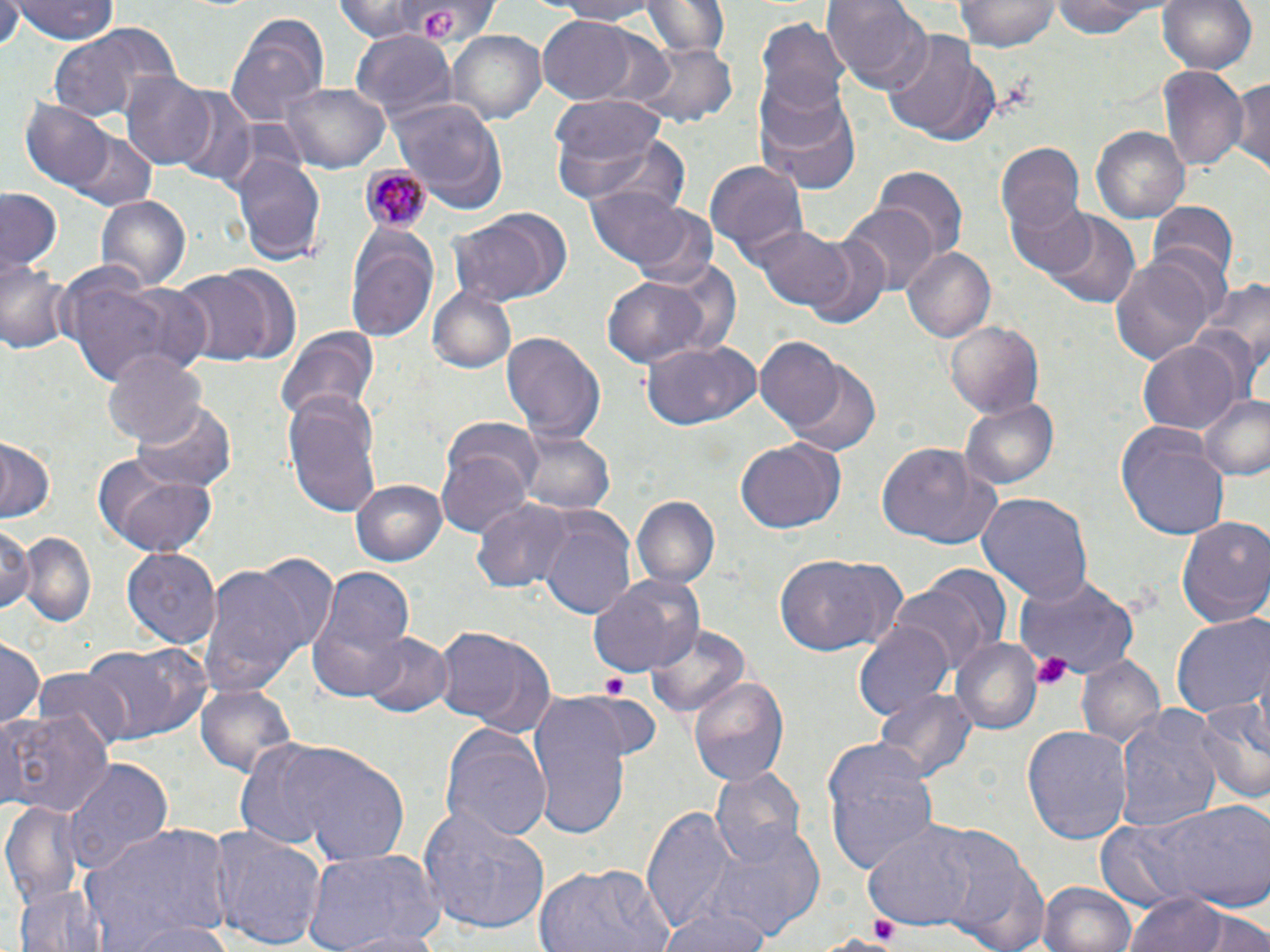

slide-level diagnosis = Plasmodium malariae
magnification = 1000x
platelet locations = approximate bounding boxes as (x1, y1, x2, y2) in pixels: (422, 7, 461, 41), (1034, 651, 1074, 690), (601, 673, 631, 696), (869, 914, 902, 946)
Plasmodium malariae-infected red blood cell locations = approximate bounding boxes as (x1, y1, x2, y2) in pixels: (361, 168, 429, 235)
stain = May-Grünwald-Giemsa
modality = light microscopy
field of view = single
uninfected red blood cell locations = approximate bounding boxes as (x1, y1, x2, y2) in pixels: (328, 0, 471, 43), (548, 0, 671, 25), (644, 0, 728, 58), (823, 0, 931, 93), (957, 0, 1061, 52), (1048, 0, 1172, 39), (1159, 0, 1257, 77), (9, 1, 121, 45), (0, 4, 24, 50), (225, 11, 331, 126), (537, 16, 642, 103), (755, 20, 850, 119), (448, 28, 549, 124), (44, 30, 149, 121), (352, 31, 454, 121), (879, 36, 997, 146), (633, 43, 736, 127), (1157, 65, 1246, 173), (1232, 71, 1270, 178), (119, 74, 216, 169), (282, 82, 390, 171), (755, 85, 862, 195), (171, 90, 256, 187), (551, 93, 669, 202), (387, 94, 507, 214), (21, 102, 113, 190), (1091, 126, 1189, 221), (580, 132, 694, 219), (64, 133, 156, 210), (994, 139, 1086, 238), (230, 149, 326, 267), (705, 159, 808, 259), (874, 164, 968, 262), (583, 183, 704, 277), (1, 190, 63, 271), (95, 195, 190, 293), (1004, 195, 1097, 280), (842, 202, 941, 293), (1151, 203, 1237, 286), (620, 205, 720, 294), (448, 209, 572, 306), (1043, 212, 1141, 307), (345, 224, 437, 339), (746, 224, 855, 313), (798, 231, 894, 331), (901, 246, 995, 344), (1108, 254, 1217, 368), (0, 256, 73, 358), (646, 258, 746, 356), (169, 263, 300, 373), (51, 265, 200, 388), (601, 274, 711, 370), (1192, 281, 1270, 402), (426, 283, 518, 374), (943, 319, 1044, 419), (274, 328, 378, 428), (502, 330, 606, 441), (753, 336, 851, 436), (642, 337, 763, 431), (1137, 338, 1243, 436), (102, 349, 206, 447), (780, 360, 882, 460), (283, 391, 383, 518), (1196, 393, 1270, 480), (960, 395, 1059, 489), (133, 401, 236, 494), (446, 419, 547, 498), (1116, 424, 1232, 541), (514, 427, 613, 518), (0, 437, 57, 522), (735, 439, 845, 533), (439, 442, 533, 537), (873, 443, 1002, 549), (94, 459, 217, 559), (353, 480, 447, 565), (976, 493, 1092, 610), (631, 494, 719, 589), (474, 500, 577, 593), (538, 509, 637, 623), (1176, 514, 1270, 628), (1, 523, 38, 616), (15, 531, 96, 630), (124, 548, 220, 650), (239, 548, 340, 657), (773, 554, 905, 659), (197, 560, 312, 696), (307, 569, 411, 699), (585, 572, 695, 679), (1013, 572, 1141, 678), (888, 581, 996, 678), (1173, 614, 1270, 719), (647, 622, 752, 722), (853, 622, 954, 725), (435, 627, 558, 737), (360, 632, 453, 718), (80, 636, 211, 744), (0, 639, 45, 725), (951, 640, 1040, 736), (1074, 653, 1164, 748), (33, 670, 135, 752), (689, 675, 789, 788), (196, 681, 296, 778), (562, 689, 656, 771), (875, 689, 977, 789), (1193, 695, 1270, 806), (528, 697, 634, 838), (0, 706, 112, 816), (1112, 707, 1226, 838), (440, 723, 552, 841), (1023, 724, 1132, 843), (238, 737, 411, 867), (822, 741, 940, 873), (59, 757, 173, 878), (708, 766, 807, 868), (1112, 796, 1269, 916), (4, 799, 88, 909), (638, 804, 749, 930), (416, 807, 552, 936), (700, 820, 825, 937), (861, 821, 990, 932), (80, 823, 231, 952), (207, 826, 329, 950), (933, 828, 1049, 952), (304, 844, 447, 952), (532, 862, 675, 952), (1038, 880, 1138, 952), (14, 883, 107, 952), (1119, 893, 1262, 952), (654, 904, 776, 952), (1183, 906, 1270, 952), (119, 920, 240, 952), (328, 928, 452, 951)
preparation = thin blood smear
image size = 1270×952 pixels